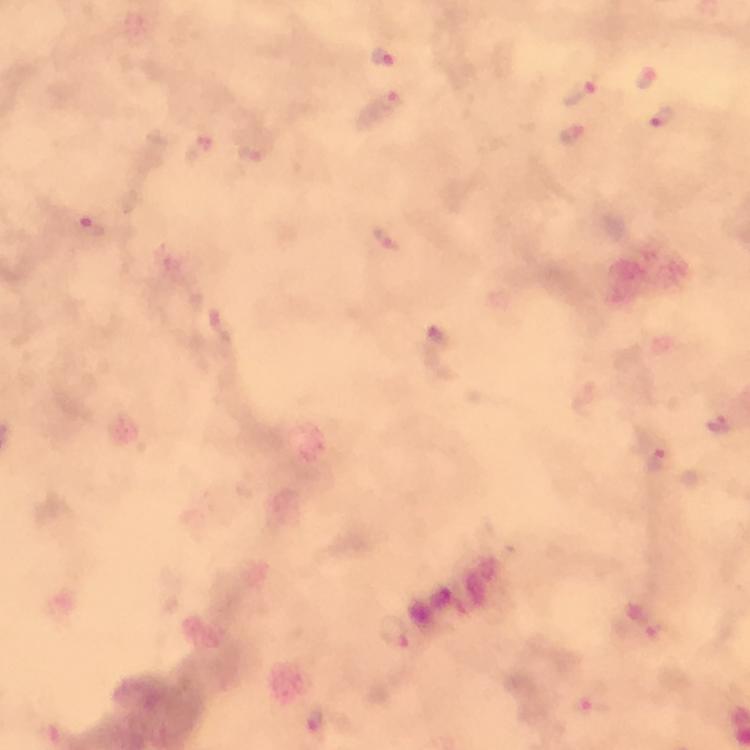 Approximate object centers, in pixels from the top-left corner. Malaria parasite locations: (x=382, y=55), (x=646, y=76), (x=579, y=92), (x=391, y=101), (x=664, y=122), (x=573, y=135), (x=195, y=150), (x=86, y=225), (x=385, y=238), (x=717, y=424), (x=657, y=461), (x=395, y=635), (x=587, y=702). Giemsa stain. A crop from one field of view. Image is 750×750 pixels. Smartphone photograph taken through a microscope. At 100x magnification. Thick blood smear. From a malaria diagnostic workup. Immersion oil was used.